Name the cell type shown.
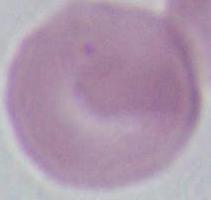

This is an erythrocyte.

Summary:
  - Modality: micrograph
  - Magnification: 1000x